Locate every Plasmodium parasite.
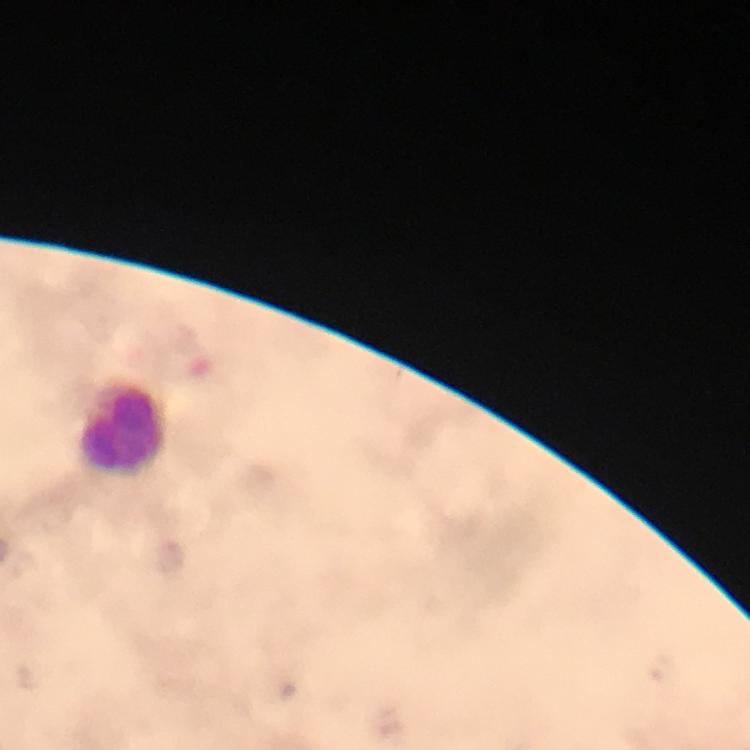

No Plasmodium parasites detected.

Approximate centers as (x, y) in pixels.
Summary:
  - Leukocyte locations: (122, 427)
  - Preparation: thick blood film
  - Stain: Giemsa
  - Image size: 750×750 pixels
  - Magnification: 100x
  - Context: from a diagnostic examination for malaria
  - Immersion oil: used
  - Cropped from: one field of view
  - Capture: smartphone photograph through a microscope